Name the parasite shown.
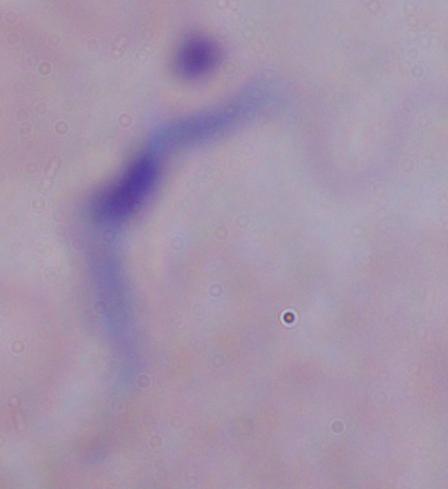
A trypanosome.

Summary:
  - Modality: photomicrograph
  - Magnification: 1000x